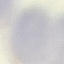 Result: negative for malaria parasites. Thin smear of blood. Cell patch, automatically extracted from a larger field of view and resized to 64 × 64 pixels. Giemsa-stained preparation. Acquired by smartphone through the microscope eyepiece.